Locate every Plasmodium parasite.
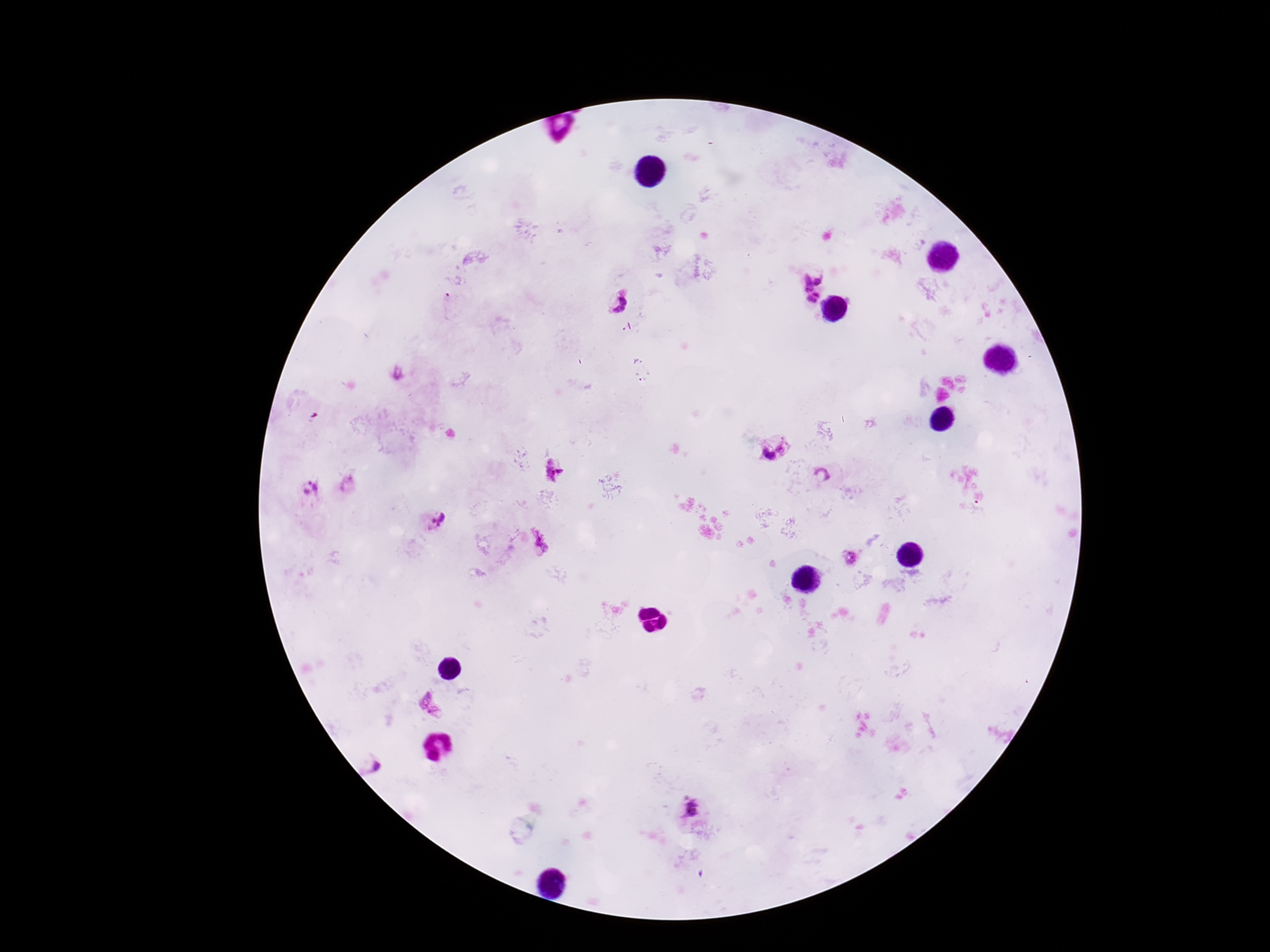
Approximate centers as (x, y) in pixels.
Plasmodium parasites: (820, 280), (805, 284), (816, 294), (811, 301), (620, 305), (784, 446), (768, 457), (555, 468), (820, 475), (312, 489), (440, 519), (544, 540), (850, 558), (420, 698), (439, 713), (377, 767), (690, 810).

Summary:
  - Stain: Giemsa
  - Capture: smartphone camera through the microscope eyepiece
  - Magnification: 100x
  - Preparation: thick blood smear
  - Patient malaria status: positive
  - Field of view: single
  - Image size: 1270×952 pixels